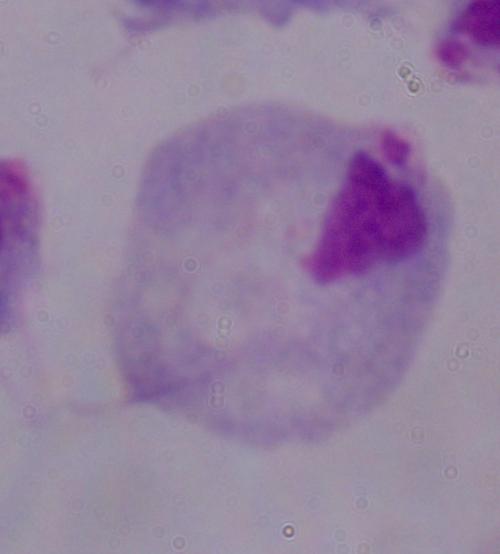
Summary:
  - Magnification: 1000x
  - Identification: trichomonad
  - Modality: photomicrograph